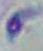
Summary:
  - Modality: photomicrograph
  - Magnification: 1000x
  - Identification: Toxoplasma gondii